Evaluate for parasitized red blood cells.
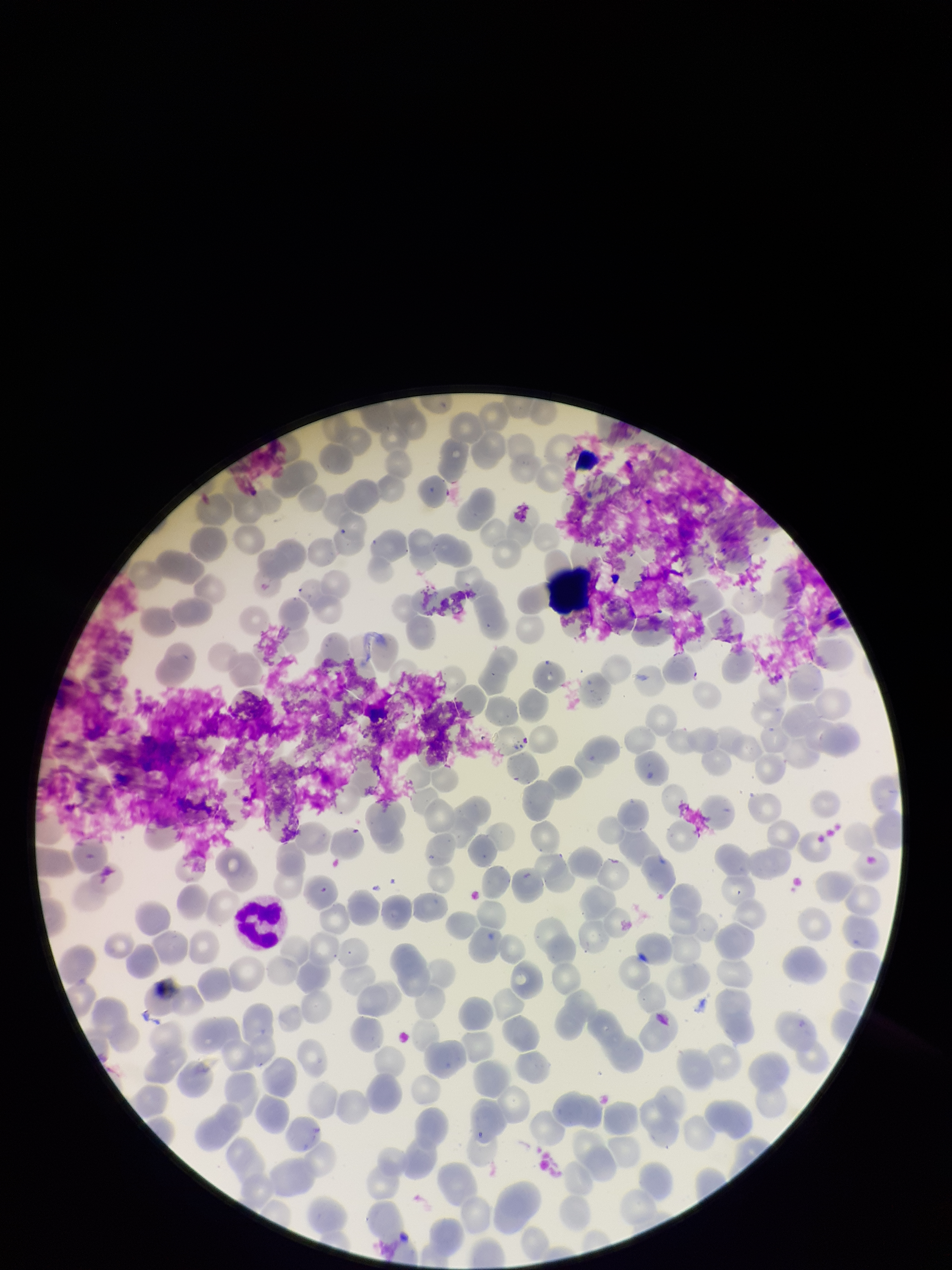

None identified.

image size = 952×1270 pixels
stain = Giemsa
capture = smartphone photograph through the microscope eyepiece
patient malaria status = negative
preparation = thin
parasitized red blood cell count = 0
field of view = single
red blood cell count = 268